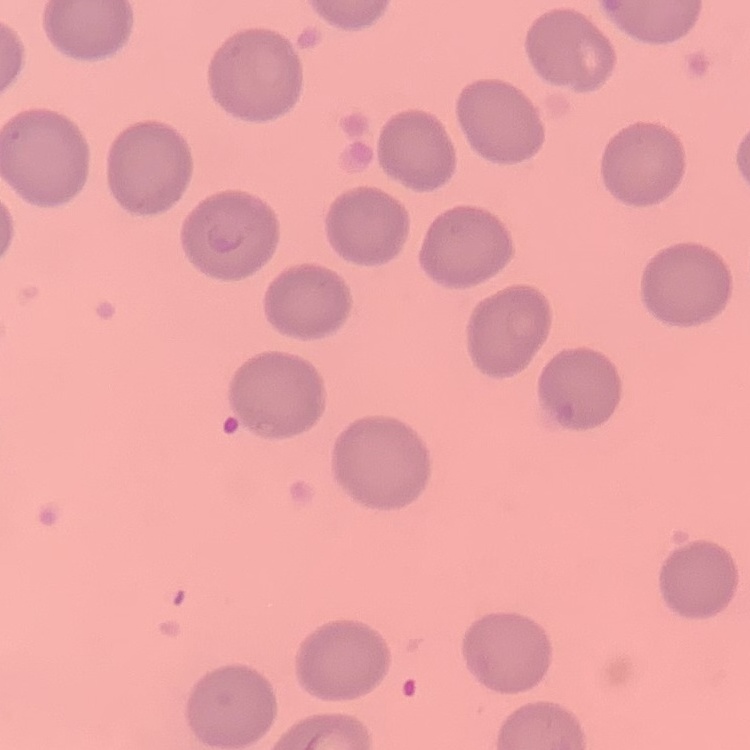
red blood cell morphology = no rouleaux formation
stain = Field's or Giemsa
image type = one tile cut from a larger photomicrograph
preparation = thin blood film